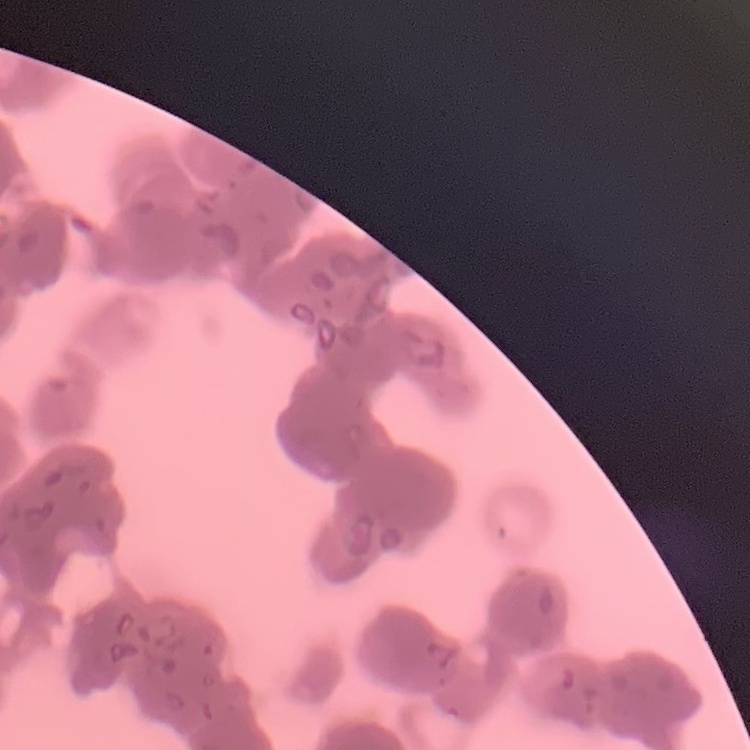 The red blood cells show rouleaux formation. Square crop of a larger photomicrograph. Thin peripheral smear. Stained with either Field's or Giemsa.